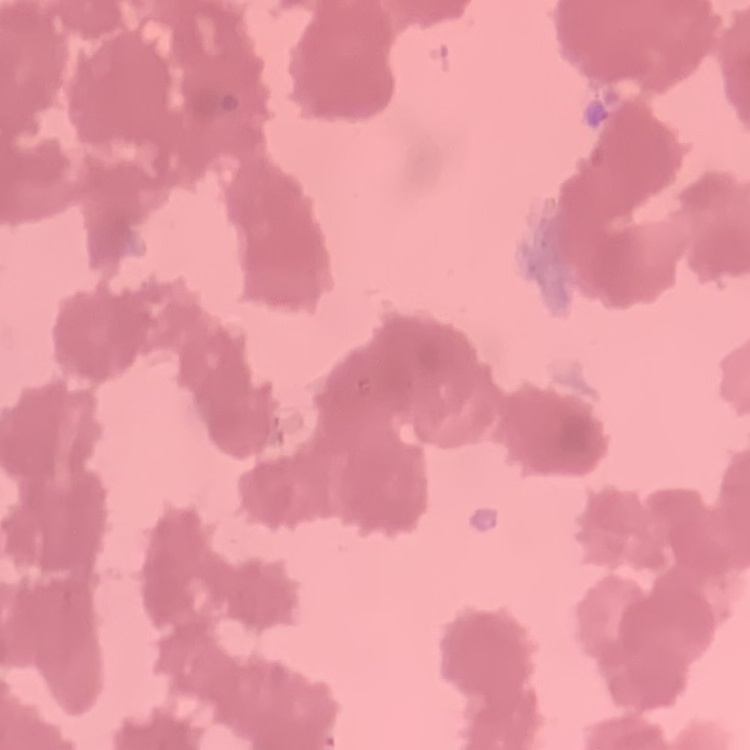

The red blood cells exhibit rouleaux formation. Stained with either Field's or Giemsa. One tile cut from a larger photomicrograph. Thin blood film.